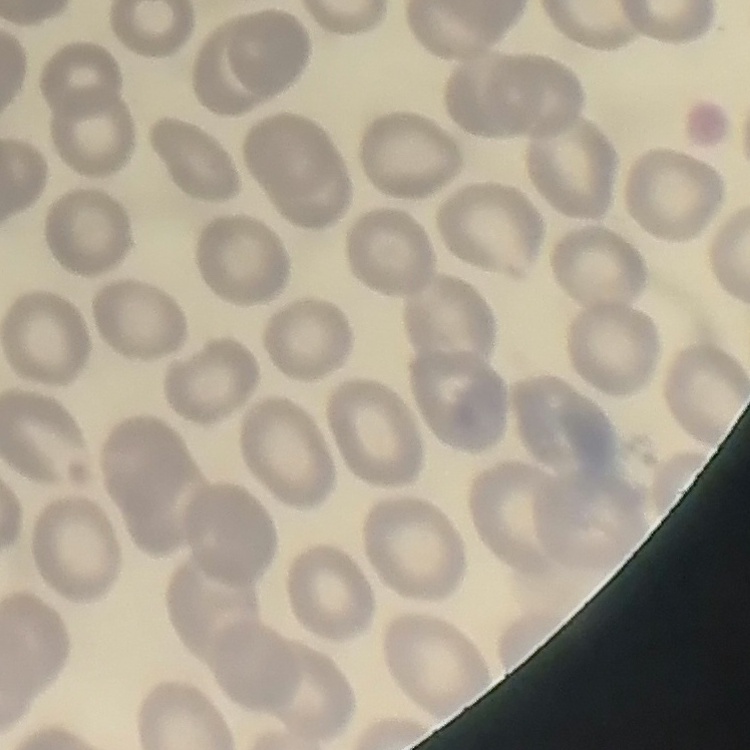
red blood cell morphology = no rouleaux formation
stain = Field's or Giemsa
image type = square crop of a larger photomicrograph
preparation = thin blood film